Evaluate for parasitized red blood cells.
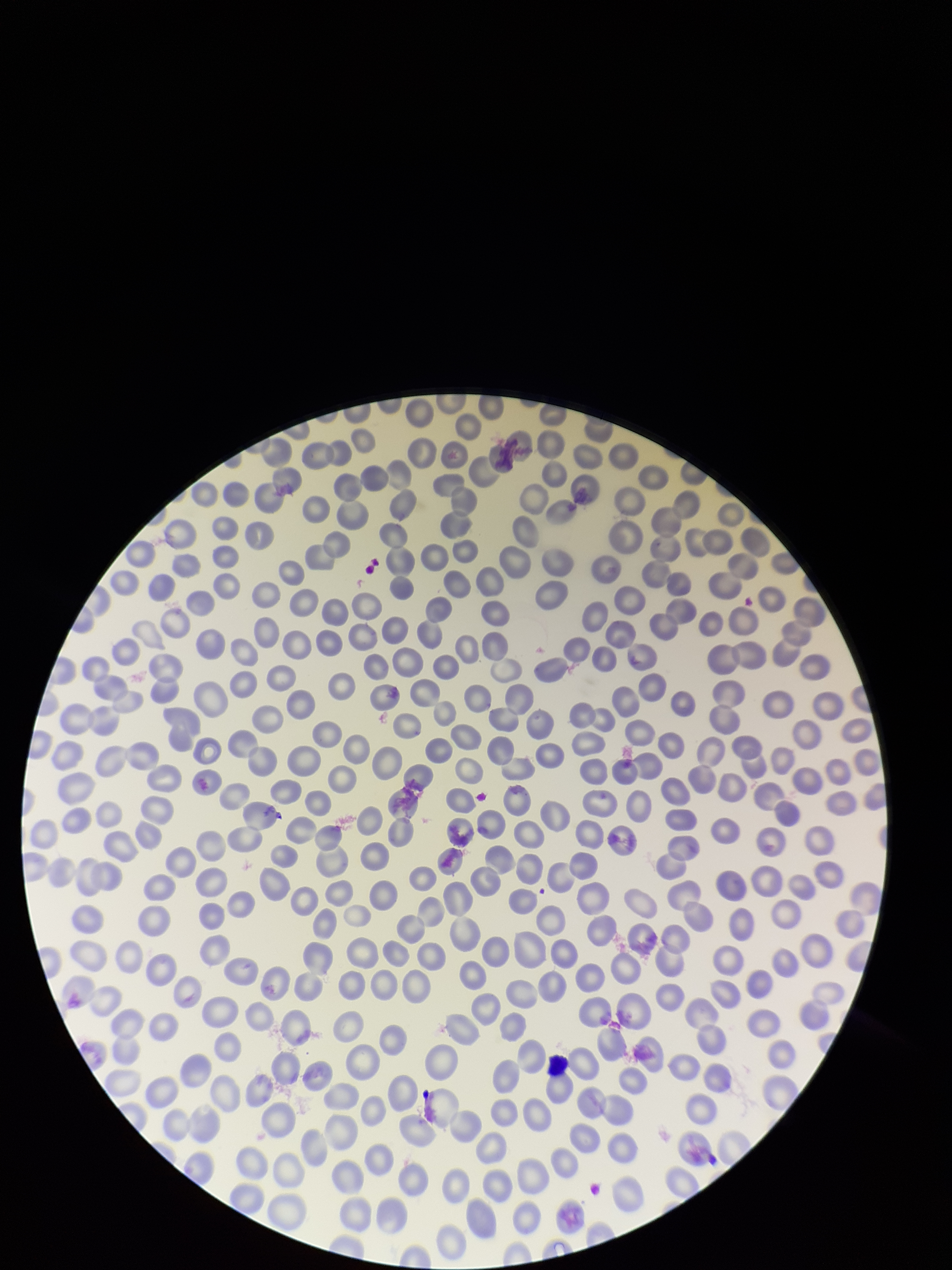
None identified.

capture = smartphone photograph through the microscope eyepiece
preparation = thin
field of view = one from this slide
patient malaria status = negative
image size = 952×1270 pixels
stain = Giemsa
red blood cell count = 308
parasitized red blood cell count = 0